Assess for malaria.
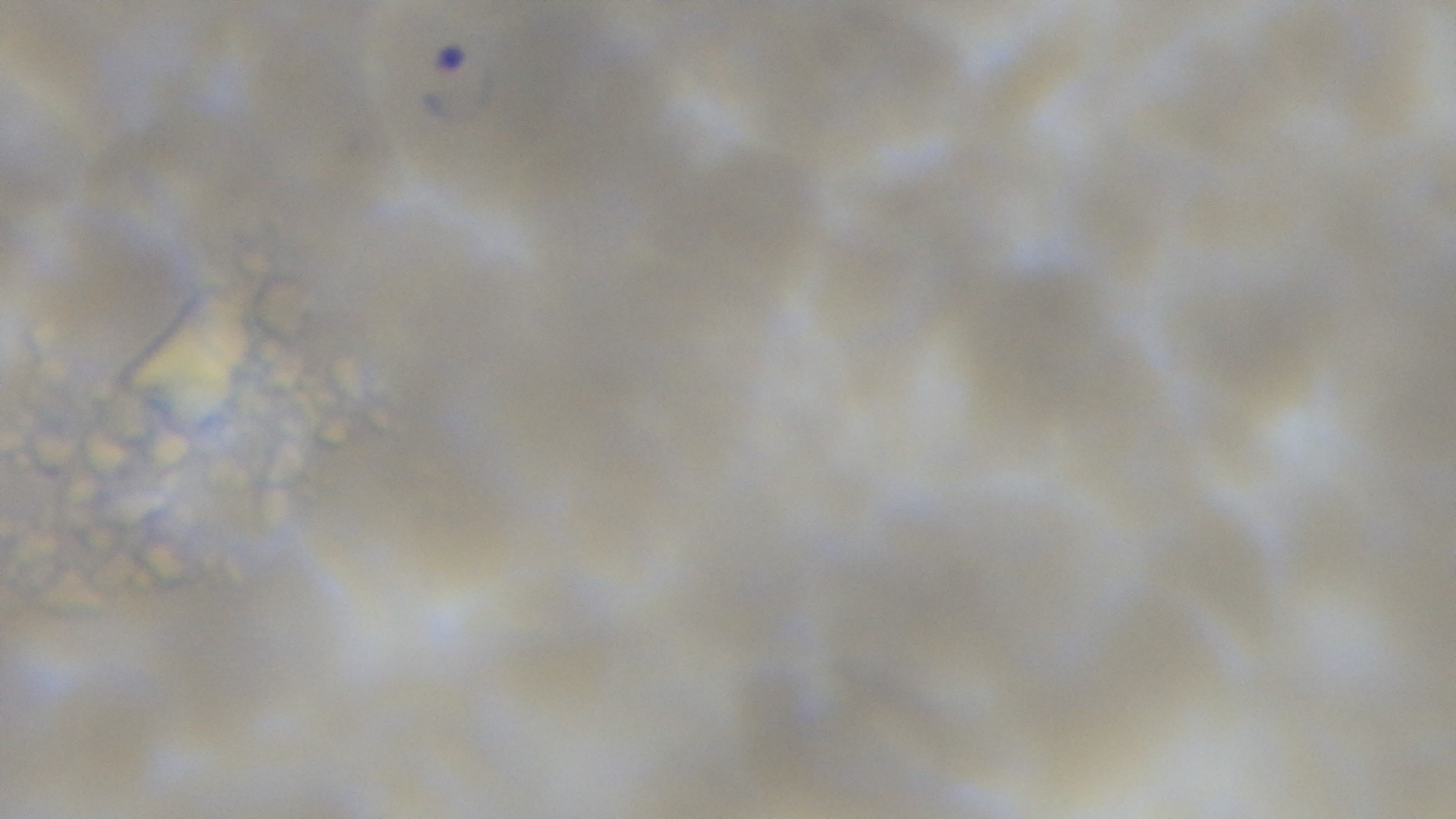

Positive.

Summary:
  - Objective: 100x oil immersion
  - Preparation: thin
  - Capture: mounted 4K digital camera
  - Stain: Giemsa
  - Field of view: one from the slide
  - Modality: light microscopy